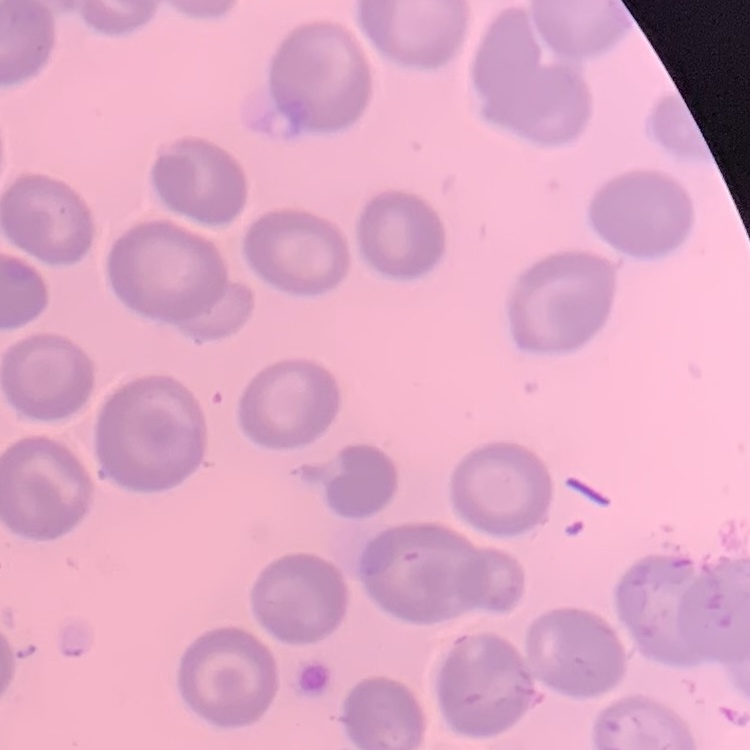

Summary:
  - Erythrocyte morphology: no rouleaux formation
  - Image type: one tile cut from a larger photomicrograph
  - Stain: Field's or Giemsa
  - Preparation: thin peripheral smear